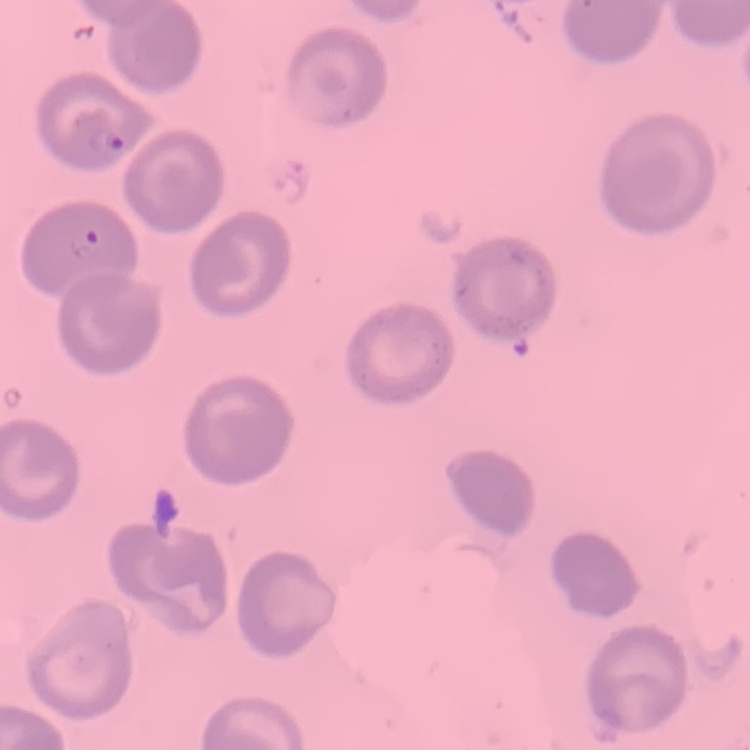 The red blood cells show no rouleaux formation. One tile cut from a larger photomicrograph. Thin peripheral smear. Field's or Giemsa stain.